Classify this cell by malaria status.
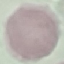

Uninfected.

Automatically extracted cell patch, resized to 64 × 64 pixels. Acquired by smartphone through the microscope eyepiece. Giemsa-stained preparation. Thin blood film.